Classify this cell by malaria status.
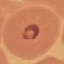
It is parasitized.

Thin blood smear. Acquired by smartphone through the microscope eyepiece. Giemsa-stained preparation. Cell patch, automatically extracted from a larger field of view and resized to 64 × 64 pixels.